Assess for malaria.
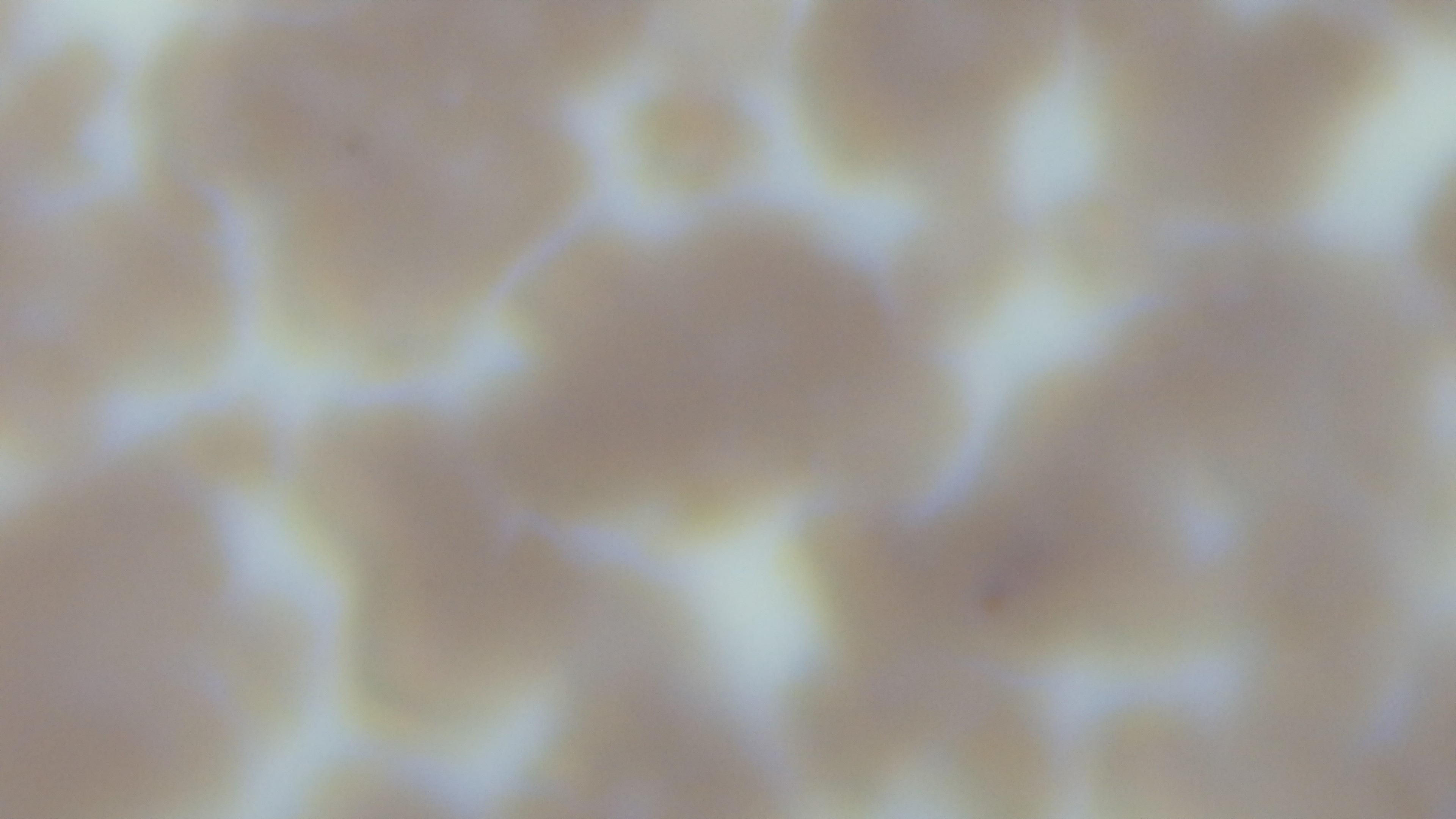
Infected.

{
  "objective": "100x oil immersion",
  "preparation": "thin smear",
  "field_of_view": "single",
  "stain": "Giemsa",
  "modality": "light microscopy",
  "capture": "mounted 4K digital camera"
}